Classify this cell by malaria status.
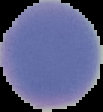

It is uninfected.

image type = cell region segmented out of the field of view; surrounding area masked to black
preparation = thin blood smear
image size = 103×112 pixels